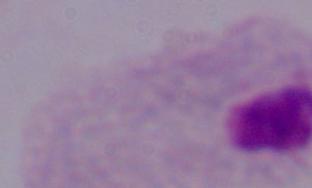
modality = photomicrograph
magnification = 1000x
identification = trichomonad